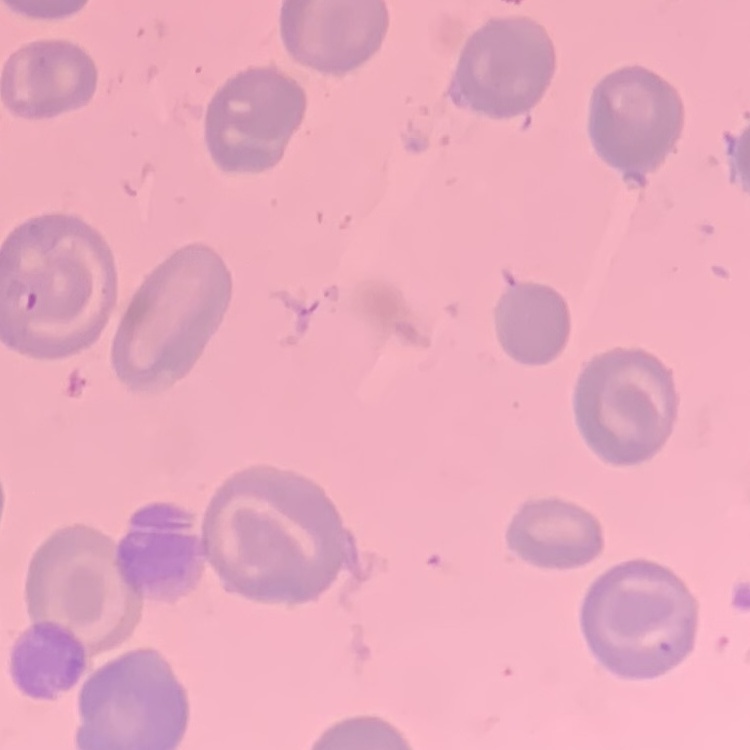 The erythrocytes exhibit no rouleaux formation. Field's or Giemsa stain. Thin blood film. Square crop of a larger photomicrograph.